Assess this cell for malaria.
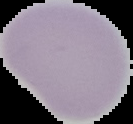
Uninfected.

preparation: thin blood smear
image_type: cell region segmented out of the field of view; surrounding area masked to black
image_size: 133×124 pixels